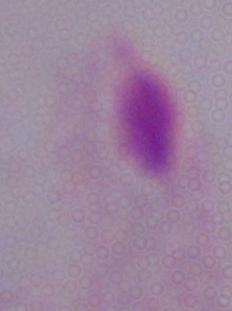
identification = trichomonad
modality = micrograph
magnification = 1000x